Give the position of every malaria parasite.
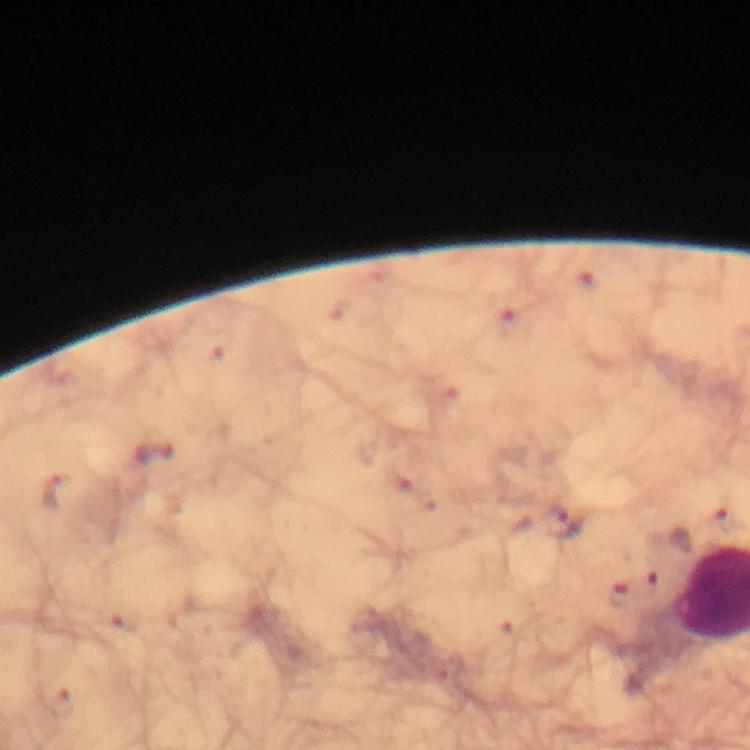

Approximate centers as [x, y] in pixels.
Malaria parasites: [154, 452], [55, 492], [566, 523], [650, 583], [617, 591].

{
  "capture": "smartphone mounted on the microscope",
  "magnification": "100x",
  "immersion_oil": "used",
  "preparation": "thick blood smear",
  "image_size": "750×750 pixels",
  "stain": "Giemsa",
  "context": "from a malaria diagnostic workup",
  "cropped_from": "a single field of view"
}